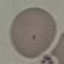

result: negative for malaria parasites
image_type: cell patch, automatically extracted from a larger field of view and resized to 64 × 64 pixels
stain: Giemsa
capture: smartphone through the microscope eyepiece
preparation: thin blood film